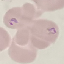
Summary:
  - Result: malaria parasites identified
  - Stain: Giemsa
  - Preparation: thin smear
  - Capture: smartphone through the microscope eyepiece
  - Image type: automatically extracted cell patch, resized to 64 × 64 pixels